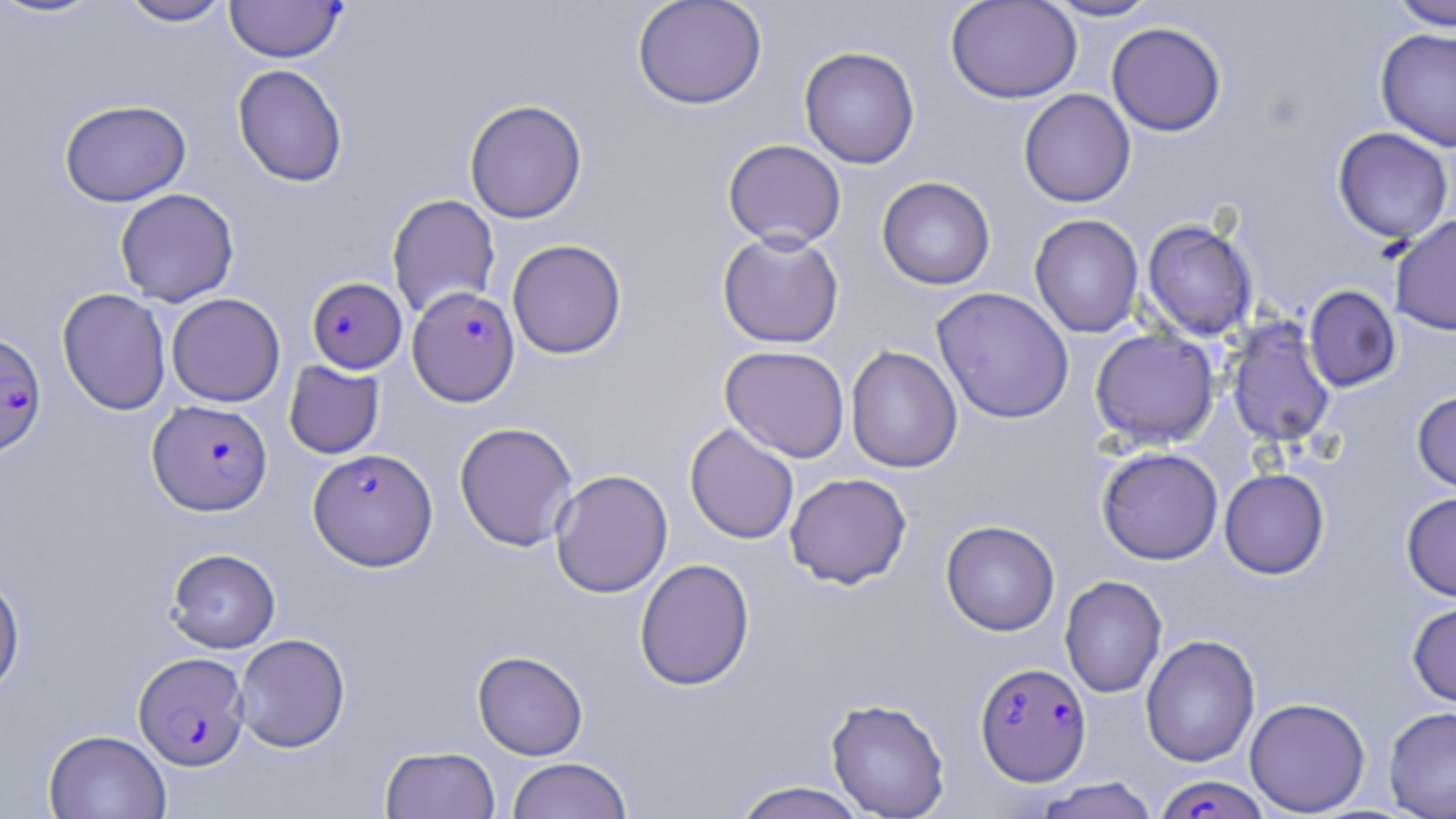
Approximate bounding boxes as named x1/y1/x2/y2 corners in pixels. Uninfected red blood cell locations: (x1=1, y1=0, x2=111, y2=21), (x1=117, y1=0, x2=234, y2=26), (x1=632, y1=0, x2=767, y2=110), (x1=945, y1=0, x2=1082, y2=104), (x1=1044, y1=0, x2=1160, y2=21), (x1=1386, y1=0, x2=1456, y2=31), (x1=1106, y1=22, x2=1226, y2=137), (x1=1375, y1=28, x2=1456, y2=151), (x1=799, y1=45, x2=920, y2=169), (x1=232, y1=64, x2=348, y2=188), (x1=1018, y1=88, x2=1136, y2=207), (x1=59, y1=99, x2=191, y2=206), (x1=464, y1=99, x2=587, y2=224), (x1=1332, y1=127, x2=1454, y2=244), (x1=722, y1=139, x2=847, y2=250), (x1=877, y1=176, x2=995, y2=290), (x1=115, y1=188, x2=239, y2=307), (x1=386, y1=194, x2=500, y2=319), (x1=1029, y1=213, x2=1144, y2=338), (x1=1389, y1=214, x2=1456, y2=336), (x1=1142, y1=219, x2=1258, y2=341), (x1=717, y1=231, x2=845, y2=348), (x1=507, y1=239, x2=627, y2=359), (x1=1304, y1=285, x2=1401, y2=392), (x1=932, y1=287, x2=1075, y2=424), (x1=57, y1=288, x2=172, y2=415), (x1=166, y1=293, x2=286, y2=407), (x1=1225, y1=317, x2=1337, y2=448), (x1=1090, y1=328, x2=1220, y2=448), (x1=720, y1=345, x2=850, y2=463), (x1=845, y1=345, x2=963, y2=473), (x1=283, y1=361, x2=384, y2=459), (x1=1411, y1=389, x2=1456, y2=494), (x1=454, y1=421, x2=579, y2=551), (x1=684, y1=423, x2=799, y2=544), (x1=1096, y1=447, x2=1223, y2=565), (x1=1219, y1=468, x2=1330, y2=579), (x1=550, y1=469, x2=673, y2=598), (x1=785, y1=473, x2=912, y2=589), (x1=1400, y1=492, x2=1456, y2=601), (x1=940, y1=520, x2=1060, y2=636), (x1=165, y1=548, x2=281, y2=653), (x1=634, y1=558, x2=755, y2=691), (x1=0, y1=572, x2=26, y2=695), (x1=1060, y1=575, x2=1167, y2=698), (x1=1407, y1=599, x2=1456, y2=707), (x1=233, y1=633, x2=351, y2=752), (x1=1140, y1=634, x2=1260, y2=767), (x1=472, y1=650, x2=588, y2=760), (x1=1244, y1=697, x2=1370, y2=816), (x1=825, y1=698, x2=950, y2=818), (x1=1384, y1=706, x2=1456, y2=818), (x1=43, y1=728, x2=172, y2=818), (x1=380, y1=745, x2=500, y2=819), (x1=506, y1=757, x2=633, y2=819), (x1=1033, y1=777, x2=1160, y2=819), (x1=730, y1=781, x2=871, y2=819). Plasmodium falciparum-infected red blood cell locations: (x1=224, y1=1, x2=347, y2=62), (x1=306, y1=276, x2=407, y2=374), (x1=407, y1=286, x2=520, y2=406), (x1=0, y1=331, x2=47, y2=458), (x1=148, y1=399, x2=273, y2=516), (x1=308, y1=447, x2=438, y2=571), (x1=134, y1=652, x2=249, y2=771), (x1=975, y1=662, x2=1091, y2=785), (x1=1154, y1=774, x2=1272, y2=818). Slide-level diagnosis: Plasmodium falciparum. Light microscopy. 1000x magnification. Image is 1456×819 pixels. May-Grünwald-Giemsa stain. Thin blood smear. One field of a larger specimen.